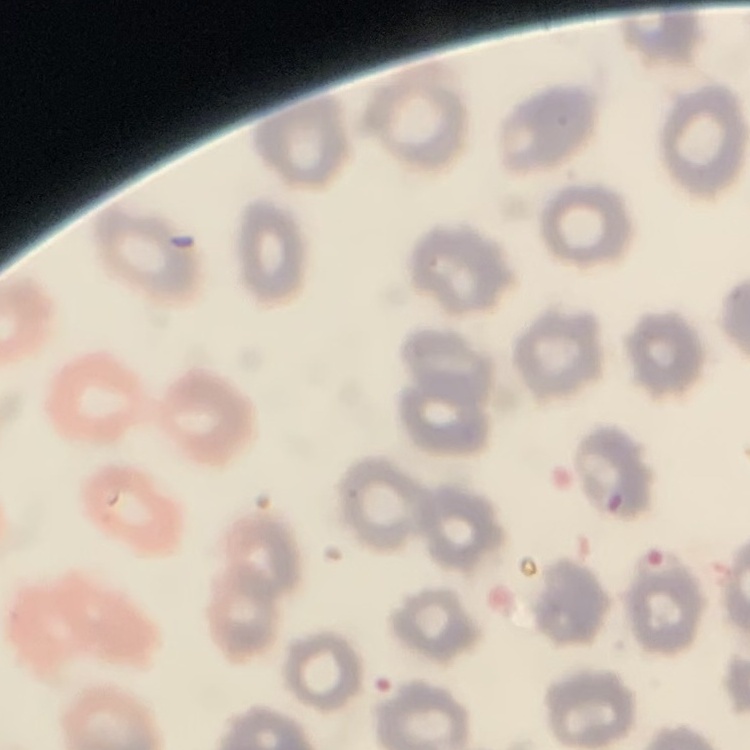
The erythrocytes show no rouleaux formation. Stained with either Field's or Giemsa. Thin blood film. One tile cut from a larger photomicrograph.